Locate every uninfected red blood cell.
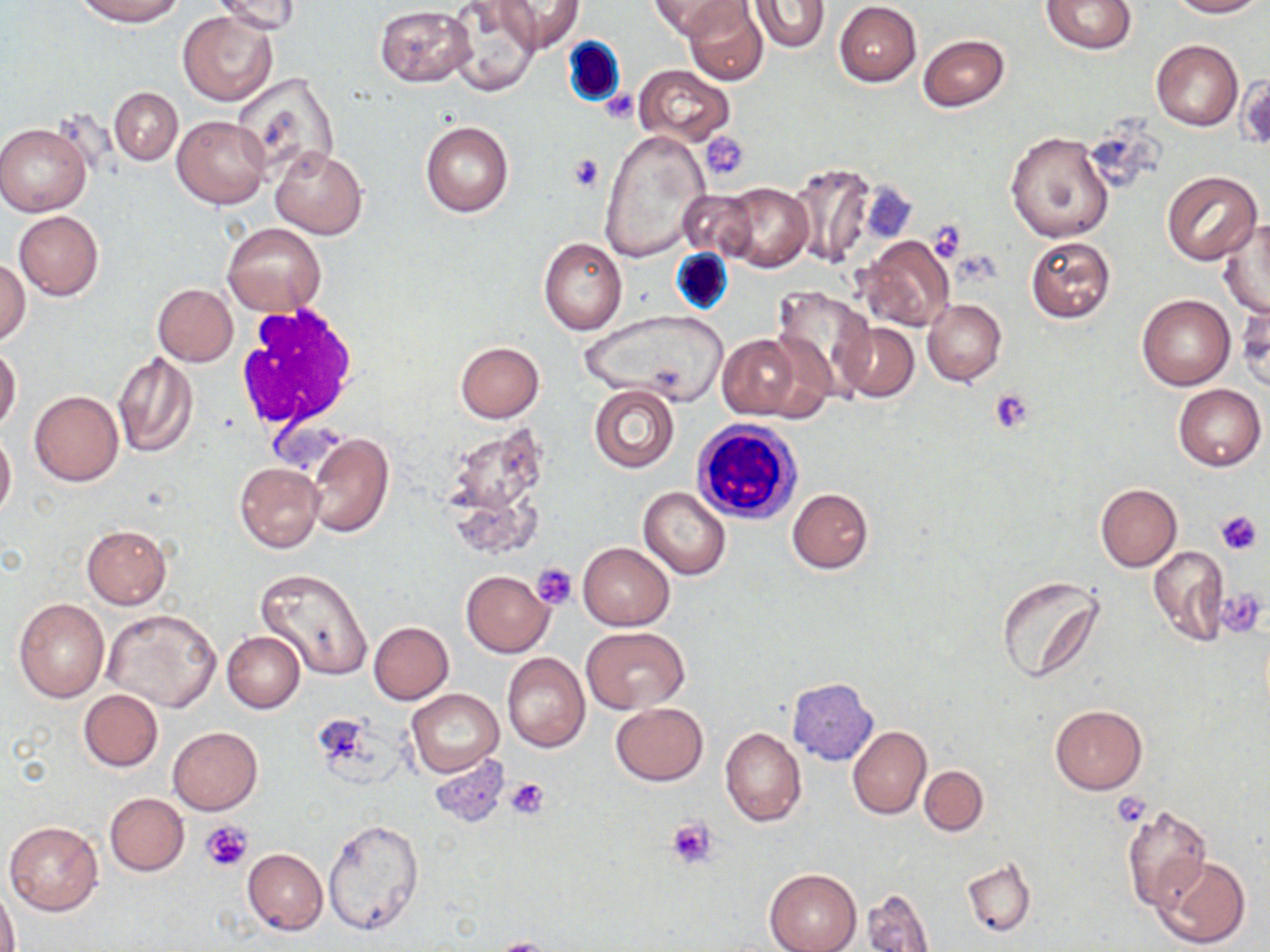
Approximate bounding boxes as named x1/y1/x2/y2 corners in pixels.
Uninfected red blood cells: (x1=648, y1=0, x2=743, y2=38), (x1=684, y1=0, x2=768, y2=85), (x1=1166, y1=0, x2=1263, y2=17), (x1=73, y1=1, x2=184, y2=27), (x1=212, y1=1, x2=304, y2=35), (x1=449, y1=1, x2=539, y2=98), (x1=495, y1=1, x2=584, y2=55), (x1=750, y1=1, x2=828, y2=52), (x1=1042, y1=1, x2=1138, y2=54), (x1=834, y1=2, x2=922, y2=86), (x1=374, y1=5, x2=474, y2=87), (x1=179, y1=12, x2=276, y2=104), (x1=918, y1=34, x2=1010, y2=112), (x1=1151, y1=40, x2=1243, y2=130), (x1=632, y1=64, x2=737, y2=146), (x1=233, y1=72, x2=340, y2=182), (x1=109, y1=87, x2=182, y2=165), (x1=172, y1=114, x2=270, y2=209), (x1=420, y1=119, x2=514, y2=218), (x1=0, y1=121, x2=92, y2=216), (x1=600, y1=129, x2=710, y2=264), (x1=1005, y1=130, x2=1113, y2=243), (x1=271, y1=147, x2=368, y2=239), (x1=787, y1=163, x2=876, y2=268), (x1=1162, y1=170, x2=1263, y2=264), (x1=714, y1=181, x2=813, y2=272), (x1=675, y1=187, x2=763, y2=260), (x1=13, y1=211, x2=104, y2=300), (x1=1218, y1=220, x2=1269, y2=317), (x1=222, y1=223, x2=325, y2=314), (x1=858, y1=235, x2=956, y2=331), (x1=1025, y1=236, x2=1115, y2=324), (x1=538, y1=237, x2=627, y2=335), (x1=0, y1=258, x2=31, y2=346), (x1=152, y1=283, x2=237, y2=365), (x1=772, y1=285, x2=874, y2=398), (x1=1136, y1=294, x2=1235, y2=391), (x1=1236, y1=297, x2=1269, y2=394), (x1=923, y1=298, x2=1005, y2=386), (x1=578, y1=310, x2=731, y2=409), (x1=726, y1=310, x2=856, y2=414), (x1=836, y1=322, x2=918, y2=401), (x1=717, y1=333, x2=806, y2=420), (x1=455, y1=342, x2=544, y2=422), (x1=0, y1=345, x2=21, y2=433), (x1=113, y1=351, x2=198, y2=458), (x1=1173, y1=383, x2=1265, y2=471), (x1=590, y1=384, x2=678, y2=472), (x1=29, y1=391, x2=123, y2=486), (x1=0, y1=429, x2=16, y2=520), (x1=306, y1=431, x2=394, y2=538), (x1=235, y1=462, x2=323, y2=553), (x1=1095, y1=483, x2=1182, y2=571), (x1=639, y1=486, x2=731, y2=580), (x1=787, y1=487, x2=873, y2=574), (x1=82, y1=524, x2=172, y2=609), (x1=577, y1=543, x2=674, y2=631), (x1=1148, y1=546, x2=1229, y2=646), (x1=256, y1=568, x2=374, y2=681), (x1=461, y1=571, x2=554, y2=657), (x1=995, y1=575, x2=1105, y2=684), (x1=13, y1=598, x2=109, y2=702), (x1=104, y1=609, x2=222, y2=712), (x1=368, y1=621, x2=454, y2=705), (x1=583, y1=626, x2=688, y2=713), (x1=222, y1=630, x2=306, y2=712), (x1=502, y1=653, x2=590, y2=753), (x1=787, y1=677, x2=879, y2=765), (x1=406, y1=688, x2=504, y2=778), (x1=78, y1=689, x2=164, y2=771), (x1=610, y1=702, x2=708, y2=785), (x1=1049, y1=705, x2=1147, y2=794), (x1=168, y1=726, x2=263, y2=814), (x1=847, y1=726, x2=931, y2=819), (x1=720, y1=728, x2=807, y2=826), (x1=428, y1=755, x2=511, y2=828), (x1=919, y1=765, x2=988, y2=836), (x1=105, y1=793, x2=188, y2=875), (x1=1121, y1=804, x2=1211, y2=912), (x1=4, y1=819, x2=104, y2=916), (x1=322, y1=819, x2=425, y2=936), (x1=243, y1=848, x2=327, y2=935), (x1=1153, y1=854, x2=1252, y2=948), (x1=962, y1=859, x2=1035, y2=937), (x1=764, y1=868, x2=861, y2=952), (x1=1, y1=885, x2=18, y2=952), (x1=861, y1=887, x2=936, y2=952).

Platelet locations: (x1=703, y1=133, x2=750, y2=181), (x1=567, y1=152, x2=605, y2=193), (x1=858, y1=182, x2=918, y2=244), (x1=926, y1=220, x2=967, y2=263), (x1=991, y1=388, x2=1034, y2=433), (x1=1214, y1=509, x2=1263, y2=556), (x1=532, y1=561, x2=578, y2=609), (x1=1218, y1=586, x2=1267, y2=636), (x1=505, y1=776, x2=550, y2=819), (x1=1113, y1=791, x2=1151, y2=828), (x1=665, y1=818, x2=718, y2=869), (x1=200, y1=820, x2=252, y2=872), (x1=490, y1=938, x2=557, y2=952). White blood cell locations: (x1=234, y1=300, x2=359, y2=434), (x1=693, y1=417, x2=804, y2=526). Slide-level diagnosis: no evidence of blood parasites. Light microscopy. Image is 1270×952 pixels. Thin blood film. May-Grünwald-Giemsa-stained preparation. Captured at 1000x magnification. Single field of view.